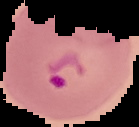 Result: malaria parasites detected. From a thin blood film. Cell region segmented out of the field of view; the surrounding area is masked to black. Image is 139×127 pixels.